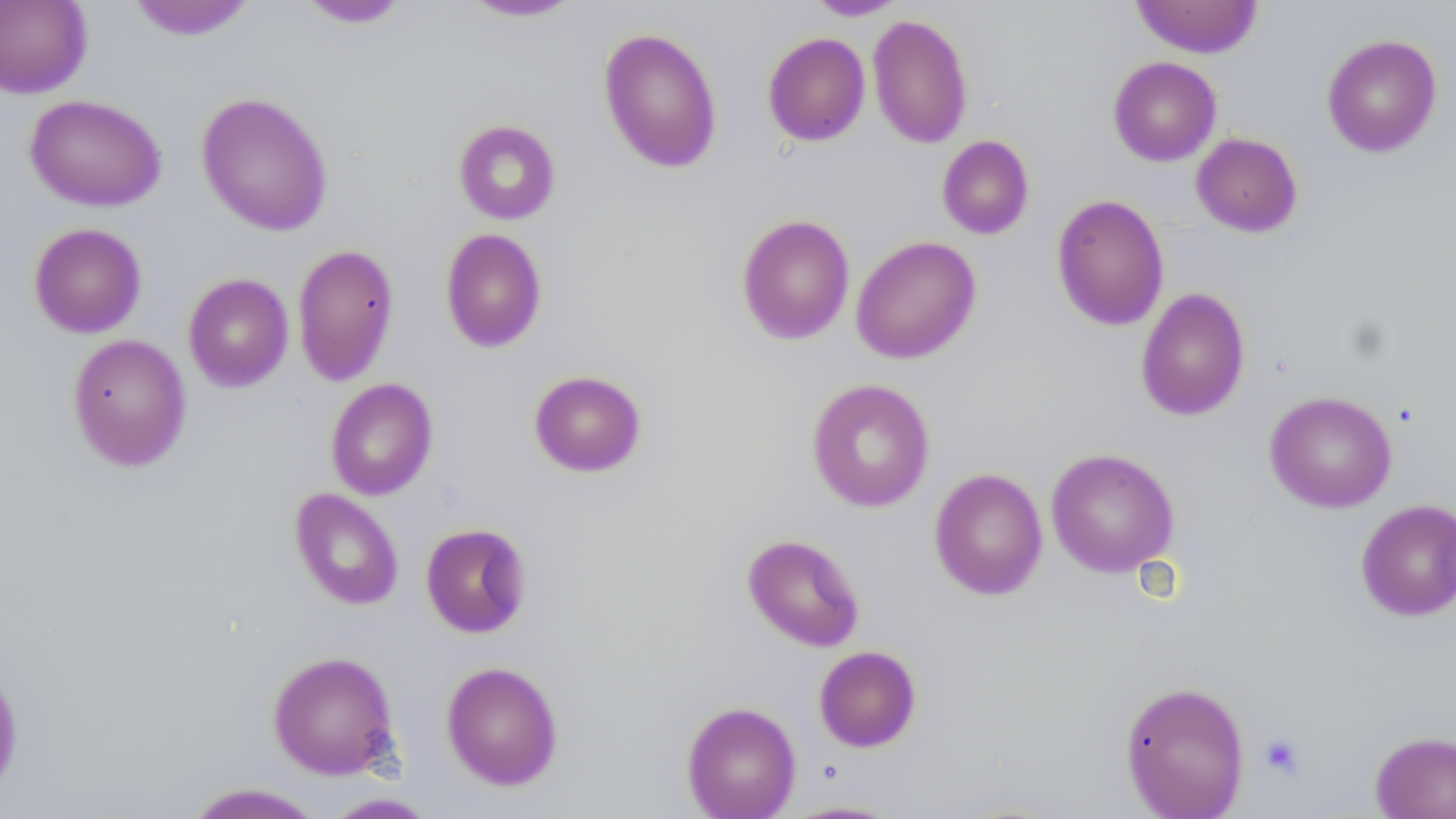

Summary:
  - Coordinate format: approximate bounding boxes as (x1, y1, x2, y2) in pixels
  - Platelet locations: (1258, 733, 1306, 780)
  - Uninfected red blood cell locations: (0, 0, 93, 98), (126, 0, 256, 41), (458, 0, 586, 23), (804, 0, 908, 20), (1130, 0, 1263, 58), (296, 1, 412, 29), (867, 14, 973, 149), (598, 27, 722, 174), (762, 32, 870, 146), (1321, 33, 1442, 158), (1107, 56, 1222, 166), (195, 91, 334, 237), (25, 94, 166, 211), (453, 119, 561, 224), (1191, 132, 1302, 236), (937, 135, 1035, 239), (1051, 194, 1169, 331), (736, 213, 855, 345), (28, 222, 147, 338), (440, 228, 547, 353), (851, 235, 982, 364), (292, 243, 400, 385), (183, 273, 294, 392), (1135, 287, 1251, 421), (67, 334, 192, 471), (528, 369, 647, 477), (325, 378, 438, 500), (806, 378, 935, 512), (1264, 390, 1397, 513), (1046, 447, 1179, 578), (929, 467, 1048, 600), (289, 488, 404, 610), (1355, 499, 1456, 622), (420, 522, 532, 638), (742, 533, 865, 652), (814, 645, 922, 752), (267, 650, 401, 780), (441, 661, 564, 791), (0, 662, 24, 799), (1119, 680, 1250, 819), (681, 701, 801, 819), (1370, 731, 1456, 819), (183, 783, 326, 819), (318, 792, 442, 818), (777, 799, 908, 818)
  - Slide-level diagnosis: no evidence of blood parasites
  - Preparation: thin blood smear
  - Magnification: 1000x
  - Image size: 1456×819 pixels
  - Field of view: one of a larger specimen
  - Modality: optical microscopy
  - Stain: May-Grünwald-Giemsa